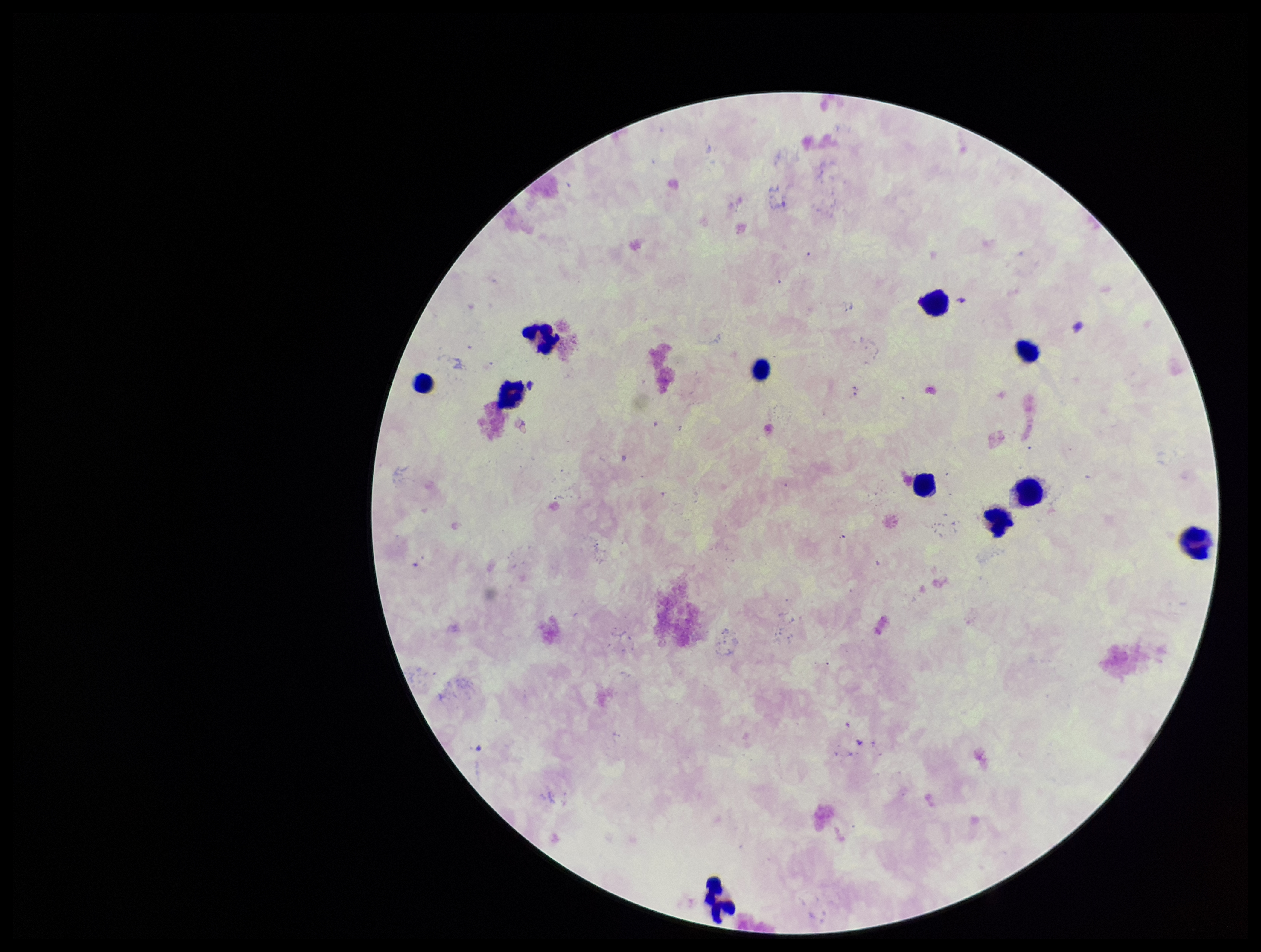
leukocyte count = 11
patient malaria status = negative
parasite count = 0
capture = smartphone photograph through the microscope eyepiece
Plasmodium parasites = none identified
image size = 1261×952 pixels
field of view = one from this slide
stain = Giemsa
preparation = thick